Locate every blood parasite and identify its species.
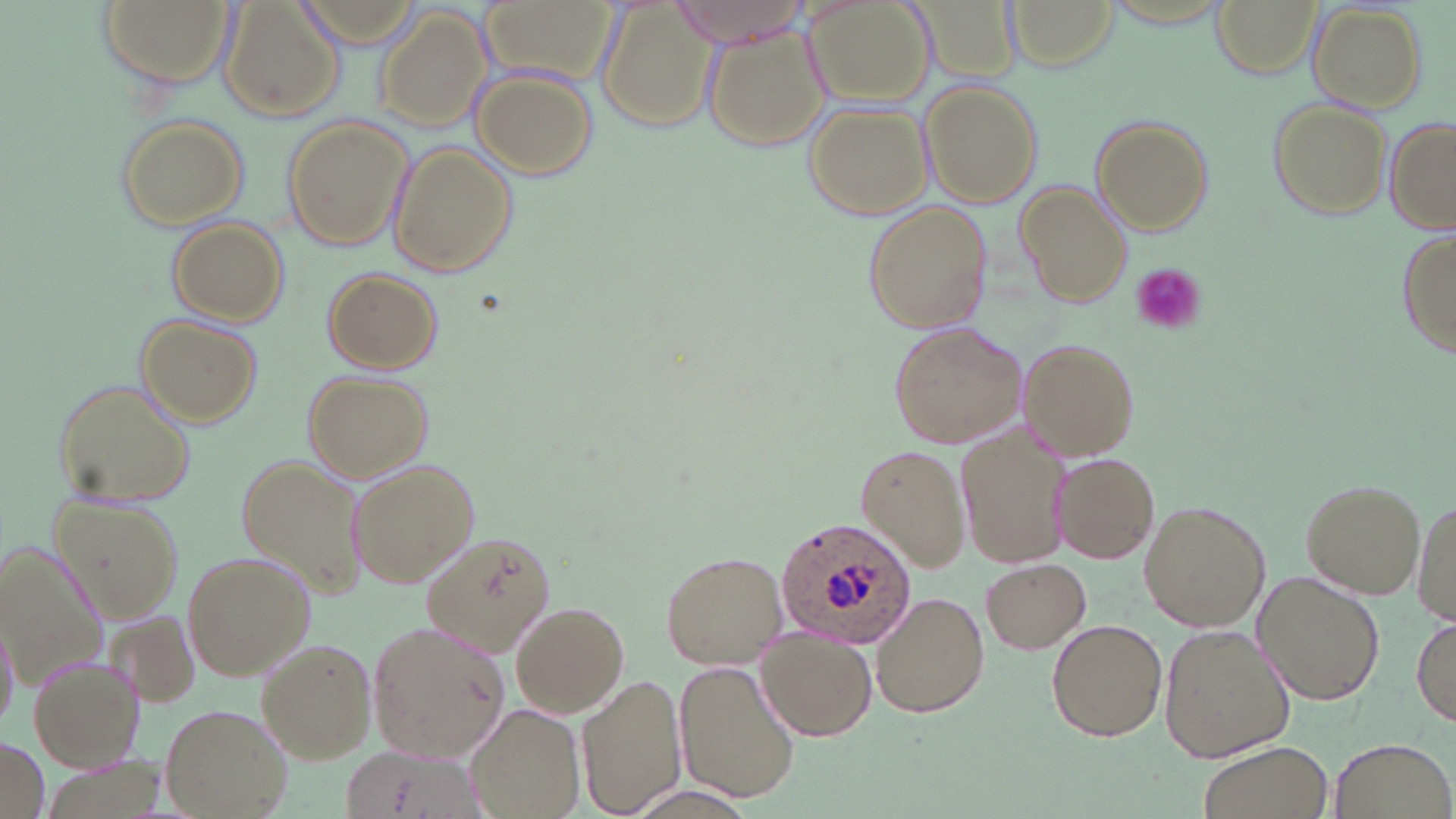

Approximate bounding boxes as (x1,y1)-(x2,y2) corner pairs in pixels.
Plasmodium ovale-infected red blood cells: (774,518)-(920,650).
No Plasmodium falciparum, Plasmodium malariae, Plasmodium vivax, Babesia divergens, or Trypanosoma brucei observed.

Summary:
  - Platelet locations: (1128,264)-(1206,335)
  - Uninfected red blood cell locations: (98,0)-(232,92), (222,0)-(344,122), (293,0)-(425,48), (484,0)-(617,84), (595,0)-(718,135), (671,0)-(809,47), (805,0)-(934,109), (1008,0)-(1120,71), (1091,0)-(1241,27), (902,1)-(1025,89), (1209,1)-(1318,77), (1310,3)-(1427,109), (373,7)-(492,132), (705,23)-(832,152), (473,67)-(598,180), (920,82)-(1042,209), (1267,98)-(1391,222), (803,102)-(931,220), (114,114)-(249,230), (280,115)-(413,252), (1092,115)-(1214,236), (1385,117)-(1456,236), (385,140)-(516,277), (1017,181)-(1129,307), (864,201)-(991,336), (165,217)-(287,327), (1395,229)-(1456,362), (322,266)-(442,374), (134,314)-(261,427), (889,320)-(1028,449), (1022,339)-(1138,459), (303,371)-(434,483), (51,377)-(196,509), (956,420)-(1069,570), (855,442)-(970,572), (1053,454)-(1160,562), (235,455)-(367,599), (346,459)-(479,589), (1298,477)-(1427,597), (48,490)-(184,621), (1414,493)-(1455,630), (1139,501)-(1270,633), (423,526)-(556,656), (1,540)-(103,686), (660,550)-(787,668), (183,552)-(312,679), (983,558)-(1091,654), (1253,570)-(1386,705), (873,590)-(990,719), (511,602)-(629,719), (0,609)-(18,736), (102,609)-(201,712), (1414,614)-(1455,729), (1047,618)-(1168,742), (366,621)-(510,764), (1158,625)-(1295,763), (756,632)-(877,741), (257,637)-(377,764), (27,653)-(144,773), (672,662)-(800,803), (577,675)-(687,819), (465,701)-(584,819), (161,703)-(293,818), (1330,736)-(1454,818), (0,738)-(48,819), (1199,741)-(1331,819), (333,744)-(482,818)
  - Slide-level diagnosis: Plasmodium ovale
  - Modality: light microscopy
  - Stain: May-Grünwald-Giemsa
  - Image size: 1456×819 pixels
  - Preparation: thin blood film
  - Field of view: single
  - Magnification: 1000x